Assess this cell for malaria.
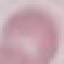

Uninfected.

Giemsa-stained preparation. Automatically extracted cell patch, resized to 64 × 64 pixels. Photographed with a smartphone camera at the microscope eyepiece. Thin blood film.